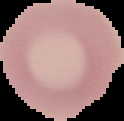
Image is 124×121 pixels. Result: negative for malaria parasites. From a thin blood smear. The area outside the segmented cell region is set to black.